Describe the morphology of the erythrocytes.
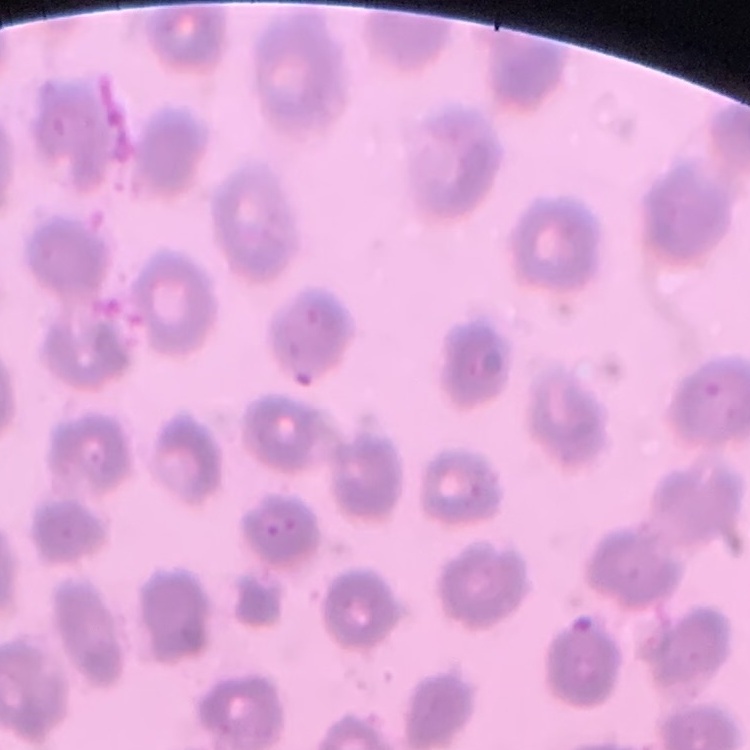
No rouleaux formation.

Square crop of a larger photomicrograph. Field's or Giemsa stain. Thin blood smear.